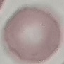
malaria_status: uninfected
stain: Giemsa
image_type: automatically extracted cell patch, resized to 64 × 64 pixels
capture: smartphone camera at the microscope eyepiece
preparation: thin blood smear